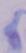
Summary:
  - Identification: trypanosome
  - Magnification: 1000x
  - Modality: photomicrograph